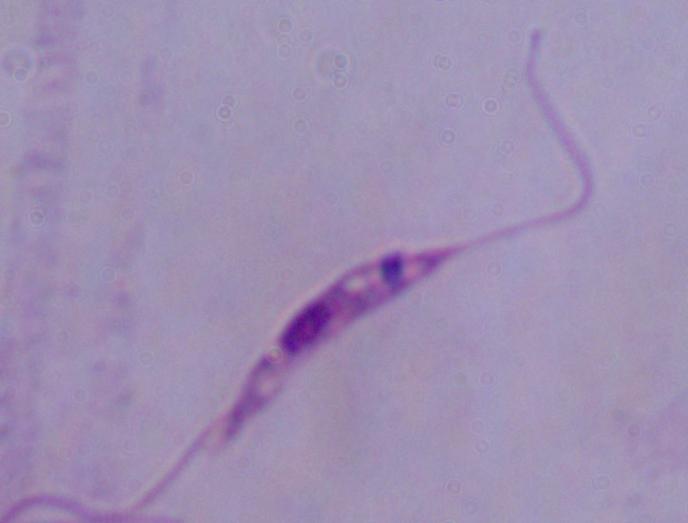

Summary:
  - Magnification: 1000x
  - Identification: Leishmania
  - Modality: micrograph